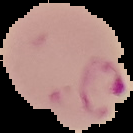

Summary:
  - Image size: 133×133 pixels
  - Preparation: thin blood smear
  - Malaria status: parasitized
  - Image type: cell region segmented out of the field of view; surrounding area masked to black